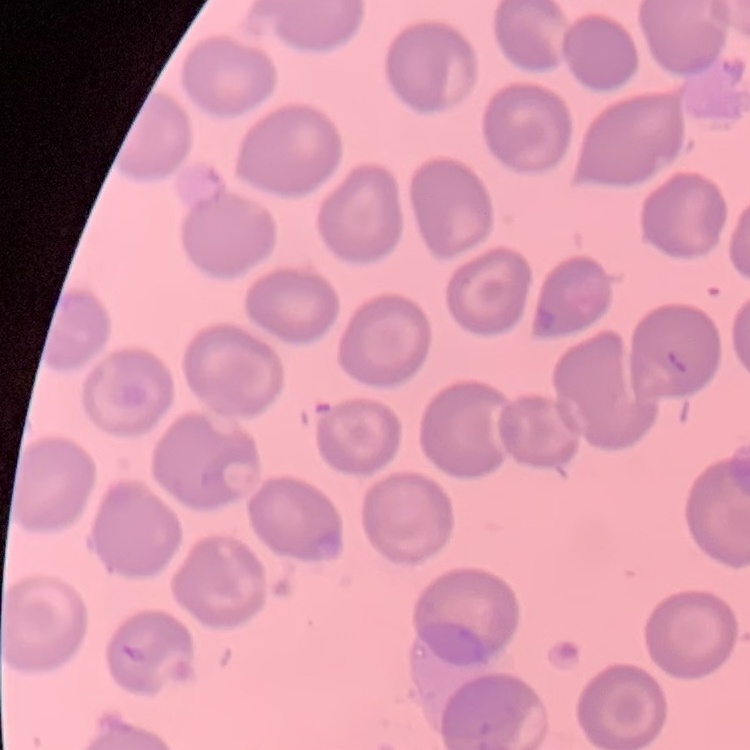

The erythrocytes exhibit no rouleaux formation. Stained with either Field's or Giemsa. One tile cut from a larger photomicrograph. Thin blood film.